Locate and identify every blood parasite.
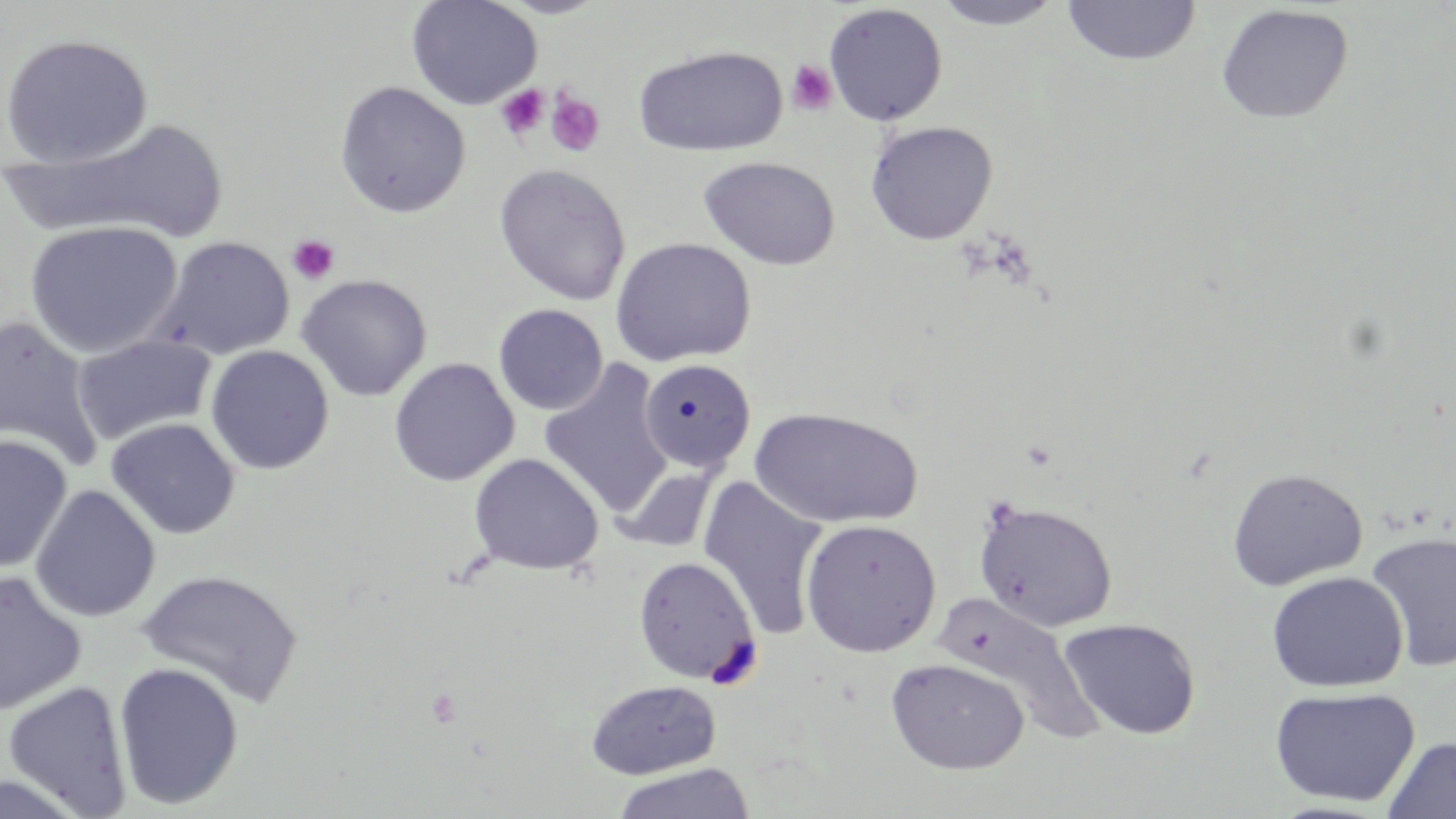

No blood parasites observed.

Approximate bounding boxes as [x1, y1, x2, y2] in pixels. Uninfected red blood cell locations: [406, 0, 542, 111], [496, 0, 611, 19], [930, 0, 1069, 31], [1060, 0, 1202, 67], [822, 3, 948, 126], [1215, 4, 1354, 124], [0, 32, 153, 168], [633, 45, 788, 157], [334, 81, 471, 218], [6, 117, 229, 247], [865, 120, 998, 245], [698, 156, 841, 271], [493, 163, 632, 306], [24, 220, 183, 358], [154, 236, 295, 360], [609, 236, 756, 367], [296, 274, 433, 401], [493, 303, 609, 415], [0, 314, 105, 473], [71, 334, 216, 446], [205, 344, 334, 474], [388, 357, 520, 487], [538, 359, 672, 517], [639, 359, 760, 476], [749, 406, 923, 529], [105, 417, 241, 539], [0, 434, 72, 574], [468, 453, 604, 575], [611, 462, 721, 554], [1226, 467, 1368, 590], [696, 474, 827, 642], [29, 484, 161, 622], [973, 498, 1118, 632], [800, 518, 941, 657], [1365, 530, 1456, 674], [633, 555, 760, 684], [136, 569, 304, 707], [0, 570, 87, 716], [1266, 570, 1408, 692], [931, 592, 1106, 746], [1059, 617, 1201, 740], [885, 657, 1030, 775], [112, 661, 245, 810], [585, 679, 721, 779], [2, 680, 133, 818], [1269, 685, 1420, 807], [1382, 735, 1456, 819], [611, 763, 756, 819]. Platelet locations: [786, 59, 838, 115], [496, 85, 549, 140], [545, 90, 605, 157], [287, 234, 340, 285]. Slide-level diagnosis: no evidence of blood parasites. One field of a larger specimen. Light microscopy. May-Grünwald-Giemsa-stained preparation. Thin blood film. 1000x magnification. Image is 1456×819 pixels.